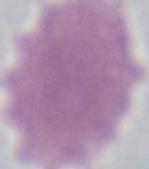

1000x magnification. Photomicrograph. An erythrocyte is shown.